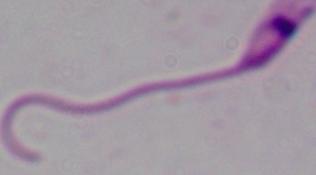
Summary:
  - Magnification: 1000x
  - Identification: Leishmania
  - Modality: micrograph